Describe the morphology of the erythrocytes.
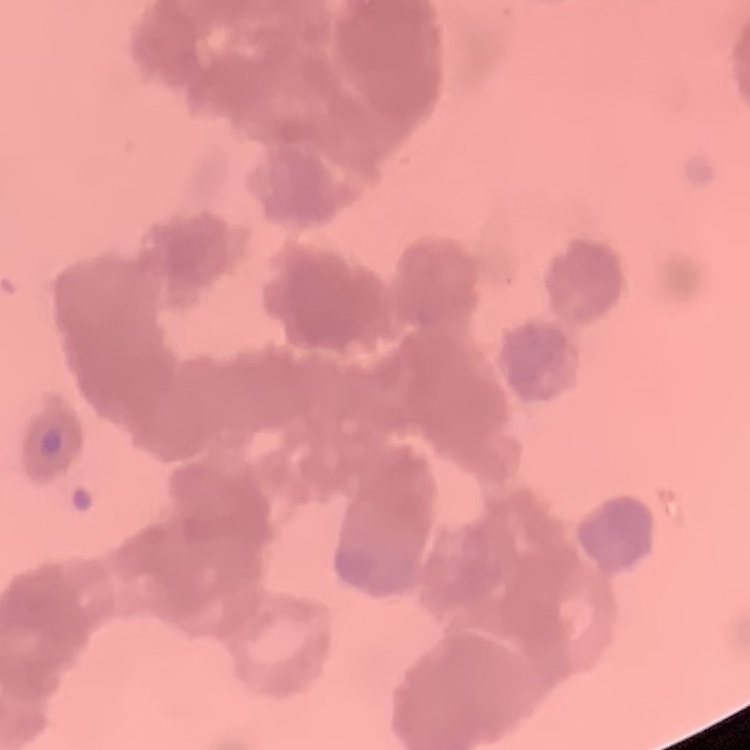
Rouleaux formation.

image_type: square crop of a larger photomicrograph
preparation: thin blood smear
stain: Field's or Giemsa